Classify this cell by malaria status.
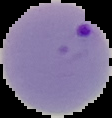

Parasitized.

image size = 112×118 pixels
preparation = thin blood smear
image type = segmented cell region on a black background